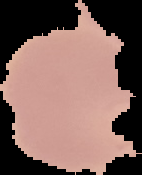
preparation: thin blood film
result: Plasmodium parasites detected
image_size: 142×175 pixels
image_type: segmented cell region on a black background